Assess this cell for malaria.
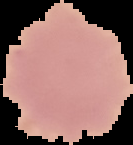

Uninfected.

Image is 133×145 pixels. Segmented cell region on a black background. From a thin blood film.